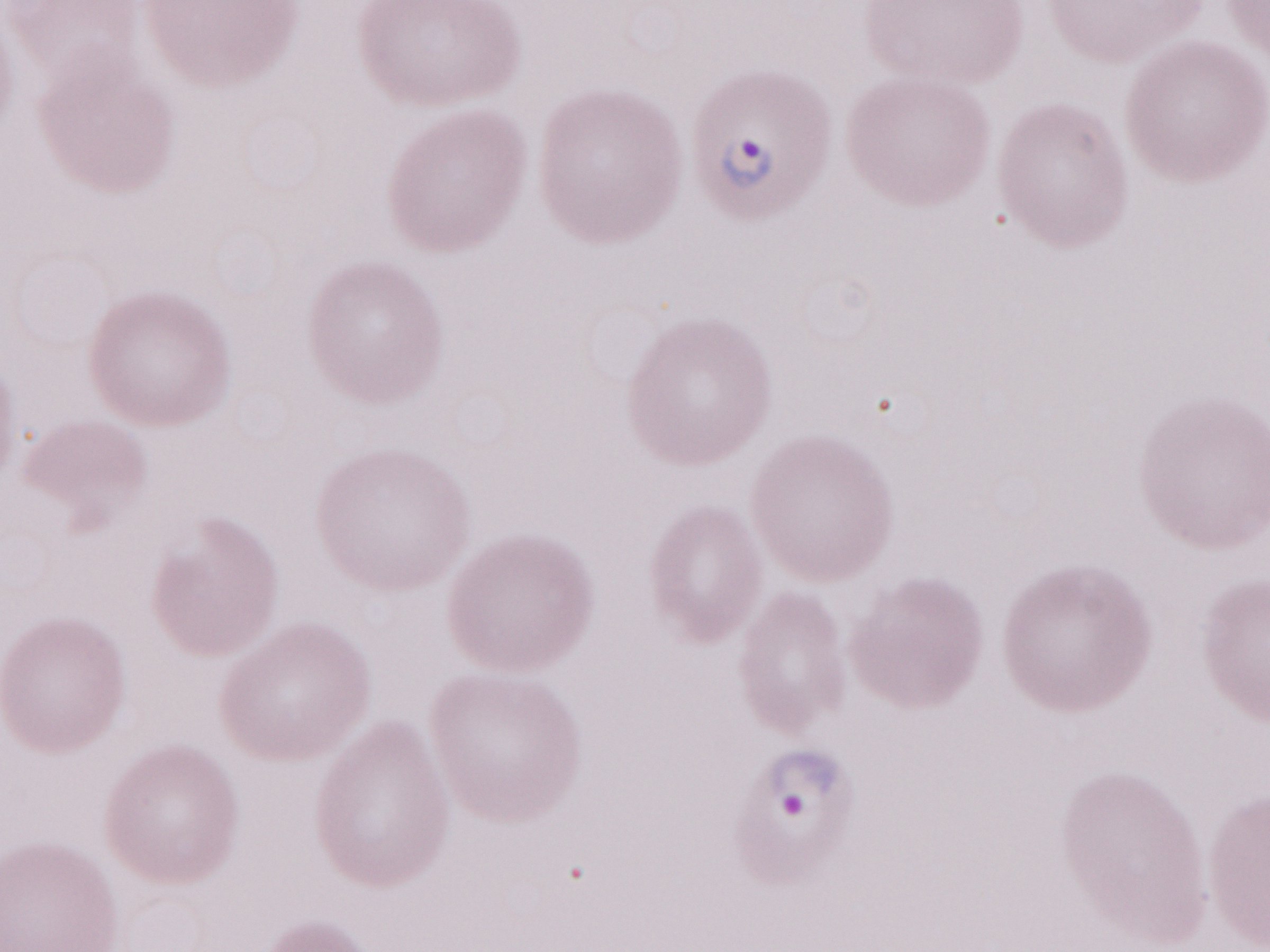
Magnification: 1,000x. May-Grünwald-Giemsa (MGG) stain. Thin blood smear. Single field of view. Image is 1270×952 pixels. Olympus BX43 microscope, Olympus DP73 camera. Patient-level malaria diagnosis: positive.